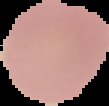
image type = segmented cell region on a black background
image size = 109×106 pixels
preparation = thin blood film
malaria status = uninfected